Report the malaria status of this cell.
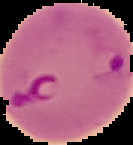

Parasitized.

Summary:
  - Preparation: thin blood smear
  - Image type: segmented cell region with the area outside set to black
  - Image size: 133×145 pixels